Outline each uninfected red blood cell.
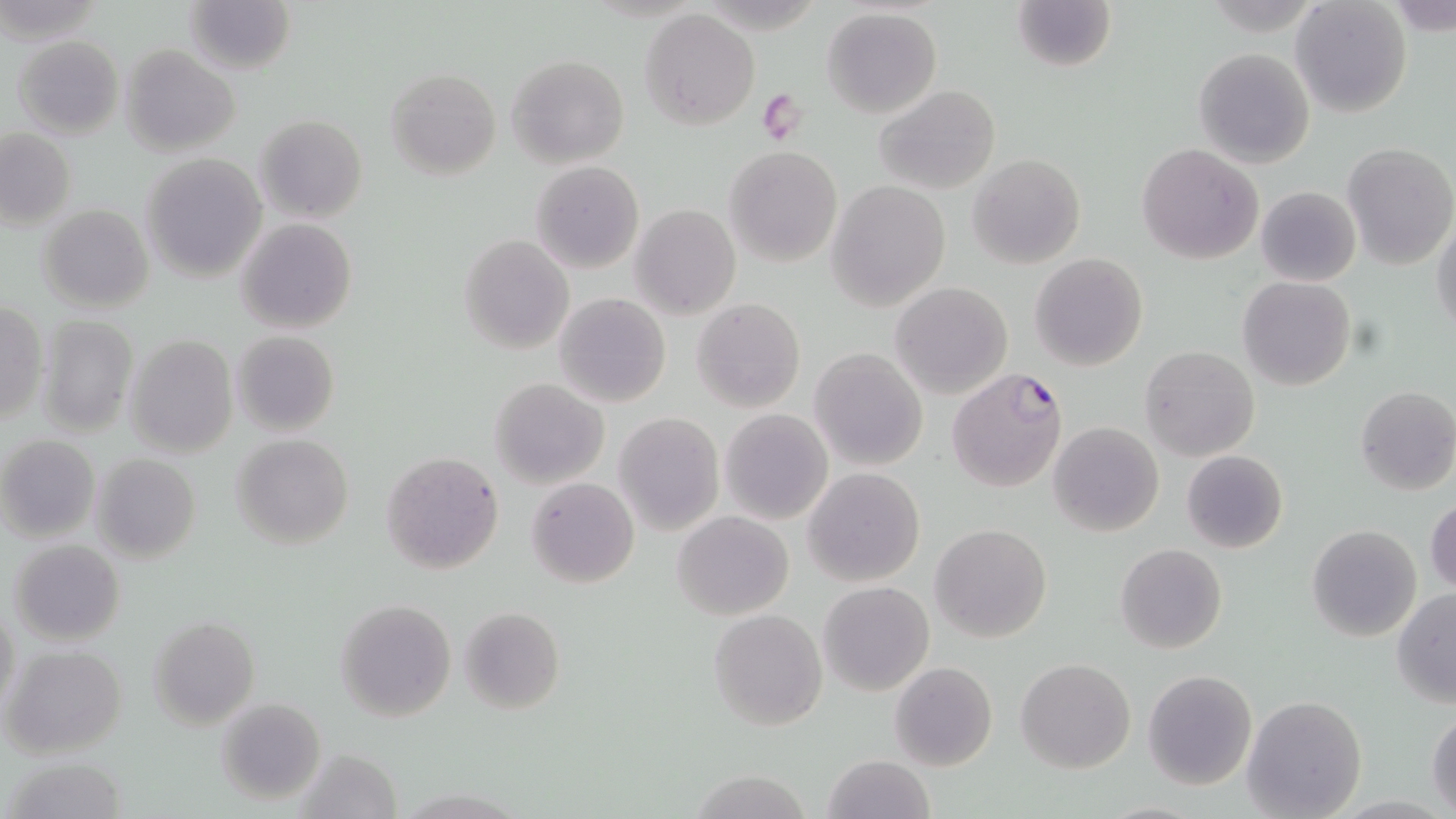

Approximate bounding boxes as [x1, y1, x2, y2] in pixels.
Uninfected red blood cells: [184, 0, 297, 76], [1010, 0, 1118, 75], [1290, 1, 1413, 118], [822, 7, 943, 119], [641, 8, 758, 129], [13, 36, 124, 137], [120, 46, 240, 156], [1193, 47, 1314, 168], [506, 54, 629, 169], [386, 68, 501, 180], [872, 85, 1000, 195], [255, 115, 367, 223], [1, 129, 76, 230], [1343, 143, 1456, 269], [1137, 144, 1264, 264], [725, 146, 842, 266], [142, 153, 266, 282], [968, 154, 1086, 270], [530, 161, 643, 274], [826, 181, 950, 311], [1255, 185, 1361, 287], [630, 203, 741, 320], [38, 204, 154, 314], [234, 218, 358, 333], [1431, 220, 1456, 338], [459, 234, 574, 354], [1030, 253, 1148, 371], [1237, 277, 1356, 391], [890, 282, 1013, 399], [554, 292, 671, 407], [691, 298, 805, 414], [0, 300, 48, 427], [36, 314, 138, 436], [231, 330, 340, 436], [123, 334, 239, 458], [1140, 345, 1260, 462], [809, 347, 928, 471], [489, 377, 609, 490], [1355, 385, 1456, 496], [719, 409, 833, 526], [615, 411, 724, 534], [1048, 422, 1163, 536], [232, 434, 355, 550], [1, 435, 99, 542], [1181, 450, 1287, 554], [381, 451, 504, 574], [93, 454, 200, 565], [804, 468, 925, 586], [525, 476, 640, 588], [1426, 498, 1456, 598], [672, 511, 794, 621], [930, 523, 1052, 643], [1305, 525, 1422, 643], [8, 538, 126, 645], [1114, 543, 1227, 654], [818, 581, 934, 697], [1391, 588, 1456, 707], [334, 599, 457, 722], [1, 604, 21, 718], [461, 607, 565, 715], [709, 609, 827, 731], [150, 617, 259, 730], [3, 644, 128, 759], [1016, 657, 1136, 774], [888, 661, 998, 771], [1142, 669, 1258, 791], [1243, 695, 1367, 819], [215, 697, 325, 805], [1427, 710, 1456, 815], [296, 746, 404, 819], [822, 754, 935, 819], [5, 757, 127, 817], [693, 771, 812, 817].

slide_level_diagnosis: Plasmodium falciparum
magnification: 1000x
plasmodium_falciparum_infected_red_blood_cell_locations: 'approximate bounding boxes as [x1, y1, x2, y2] in pixels: [946, 368, 1069, 493]'
modality: optical microscopy
platelet_locations: 'approximate bounding boxes as [x1, y1, x2, y2] in pixels: [759, 90, 806, 141]'
image_size: 1456×819 pixels
stain: May-Grünwald-Giemsa
field_of_view: one of a larger specimen
preparation: thin blood smear